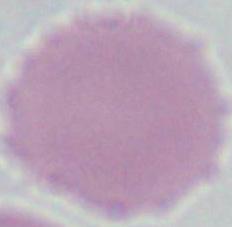

An erythrocyte is seen. Micrograph. Captured at 1000x magnification.